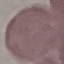
Malaria status: uninfected. Automatically extracted cell patch, resized to 64 × 64 pixels. Thin smear of blood. Giemsa-stained preparation. Acquired by smartphone through the microscope eyepiece.